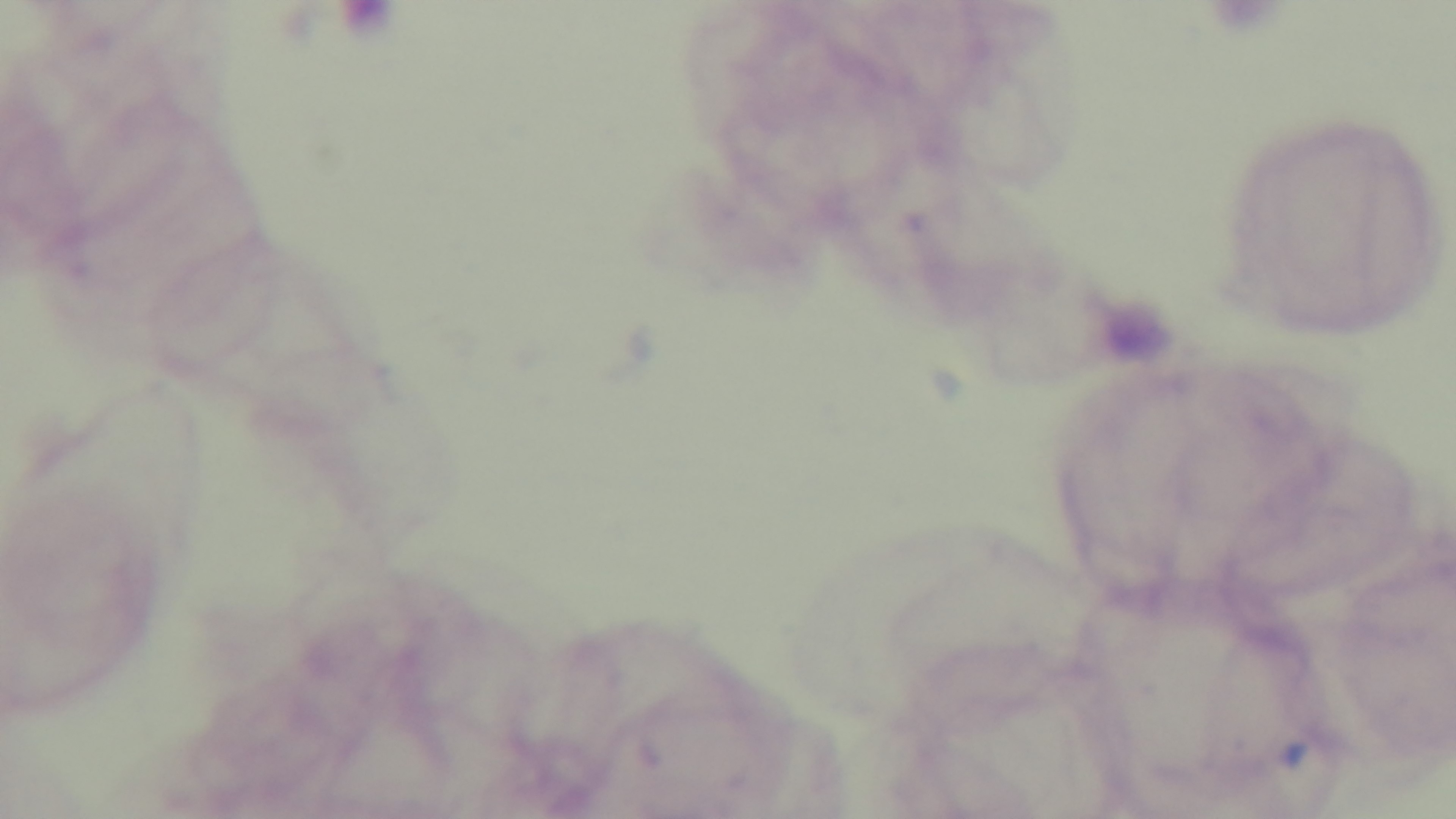 Malaria status: negative. Oil-immersion objective, 100x. Giemsa stain. Preparation: thick smear. Photomicrograph. Mounted 4K digital camera. Single field of view.